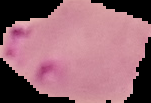
Image is 151×103 pixels. Cell region segmented out of the field of view; the surrounding area is masked to black. Malaria status: parasitized. From a thin blood film.